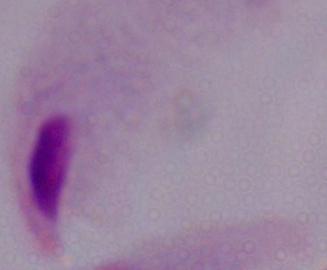
modality = micrograph
identification = trichomonad
magnification = 1000x